Give the position of every Plasmodium parasite.
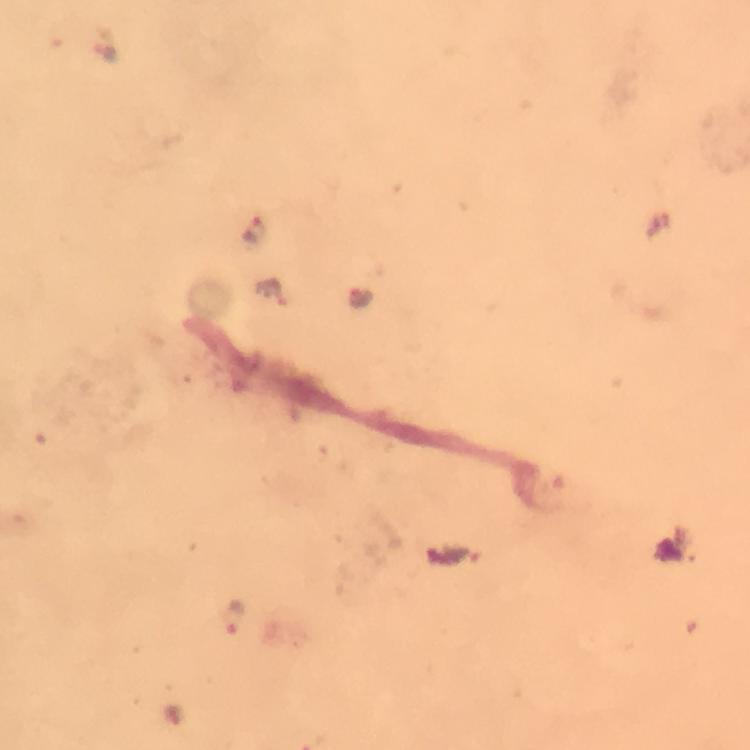
Approximate centers as (x, y) in pixels.
Plasmodium parasites: (109, 54), (271, 294), (361, 295), (233, 617).

image size = 750×750 pixels
magnification = 100x
immersion oil = used
cropped from = one field of view
preparation = thick smear
capture = smartphone camera through the microscope
context = from a malaria diagnostic workup
stain = Giemsa